Comment on the morphology of the erythrocytes.
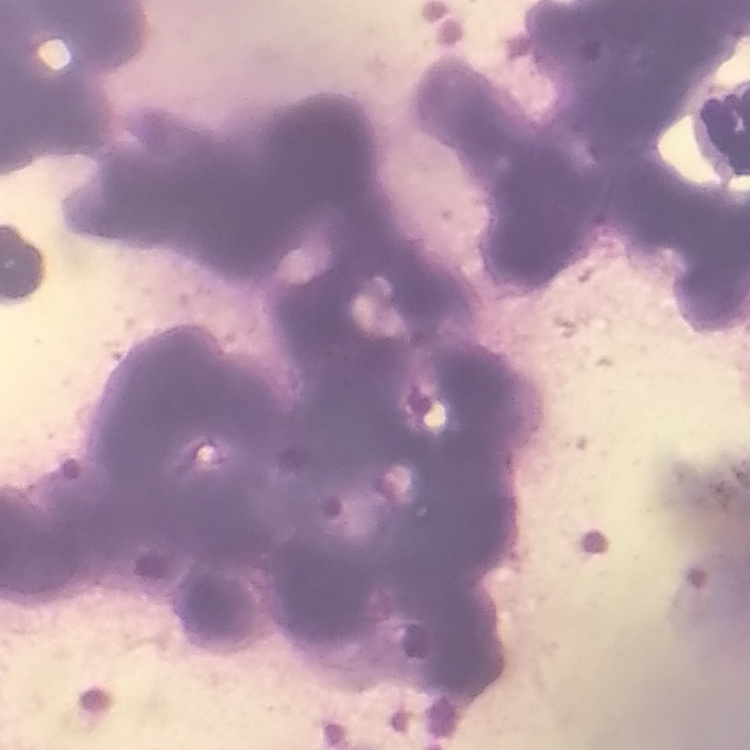

They show rouleaux formation.

Summary:
  - Image type: one tile cut from a larger photomicrograph
  - Preparation: thin peripheral smear
  - Stain: Field's or Giemsa